Give the extent of all Babesia divergens-infected red blood cells.
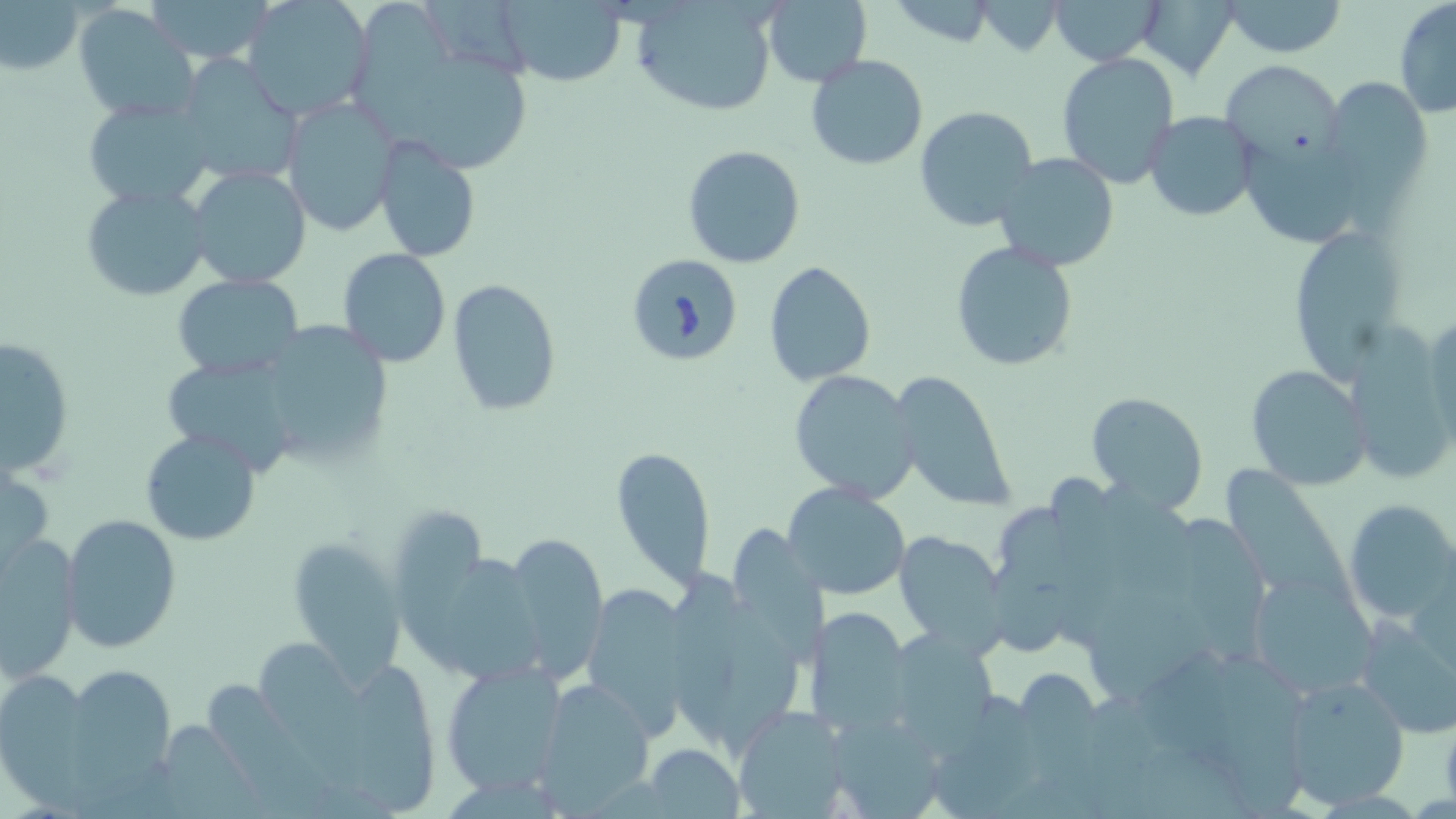
Approximate bounding boxes as (x1,y1)-(x2,y2) corner pairs in pixels.
Babesia divergens-infected red blood cells: (624,254)-(744,369).

Uninfected red blood cell locations: (143,0)-(275,64), (1050,0)-(1161,65), (1137,0)-(1237,79), (1221,0)-(1347,57), (1393,0)-(1456,120), (242,1)-(372,120), (357,1)-(465,153), (631,1)-(781,115), (887,1)-(1000,47), (975,1)-(1065,56), (2,2)-(85,76), (495,2)-(628,85), (761,3)-(870,84), (74,4)-(202,121), (1056,52)-(1180,188), (415,53)-(531,175), (805,54)-(928,171), (175,55)-(303,190), (1217,58)-(1345,171), (1319,75)-(1432,200), (282,96)-(401,233), (82,97)-(216,207), (914,106)-(1036,229), (1145,111)-(1259,222), (371,137)-(481,262), (682,143)-(807,269), (1244,144)-(1363,250), (994,153)-(1119,271), (186,164)-(313,290), (80,182)-(211,303), (1297,221)-(1403,389), (948,241)-(1078,372), (339,248)-(451,367), (763,261)-(879,388), (174,274)-(305,380), (446,279)-(561,416), (1423,306)-(1456,455), (1345,316)-(1451,481), (269,326)-(395,458), (0,335)-(75,478), (164,354)-(300,475), (1244,365)-(1368,489), (790,369)-(922,502), (891,373)-(1017,512), (1085,391)-(1208,515), (140,429)-(261,545), (611,446)-(715,590), (1,458)-(53,574), (1228,461)-(1356,607), (785,483)-(910,601), (1344,500)-(1456,623), (399,506)-(485,666), (1181,508)-(1273,663), (60,511)-(182,653), (733,522)-(828,668), (2,532)-(81,678), (893,532)-(1004,653), (503,534)-(606,677), (285,536)-(406,682), (449,551)-(548,690), (990,558)-(1081,659), (664,567)-(747,760), (1248,569)-(1376,698), (581,585)-(697,732), (1088,585)-(1220,705), (720,597)-(808,755), (805,608)-(913,737), (1354,610)-(1455,739), (896,621)-(995,760), (263,637)-(400,803), (1217,650)-(1316,819), (439,658)-(567,797), (361,662)-(437,814), (61,663)-(178,788), (1015,669)-(1103,756), (0,671)-(100,808), (211,676)-(353,819), (1279,676)-(1410,809), (536,680)-(657,811), (933,694)-(1047,819), (730,705)-(848,818), (824,714)-(952,816), (165,718)-(267,819), (642,744)-(745,819). Slide-level diagnosis: Babesia divergens. May-Grünwald-Giemsa-stained preparation. Thin blood film. Image is 1456×819 pixels. Optical microscopy. 1000x magnification. One field of a larger specimen.